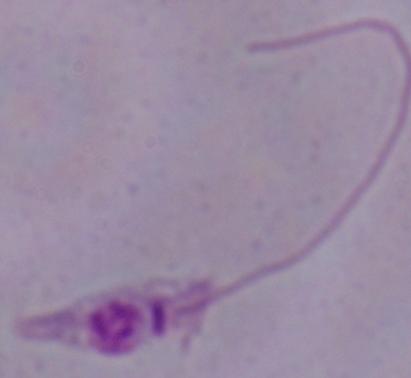

modality = micrograph
identification = Leishmania
magnification = 1000x